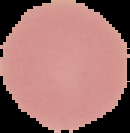

image size = 130×133 pixels
result = no malaria parasites detected
image type = cell region segmented out of the field of view; surrounding area masked to black
preparation = thin blood film